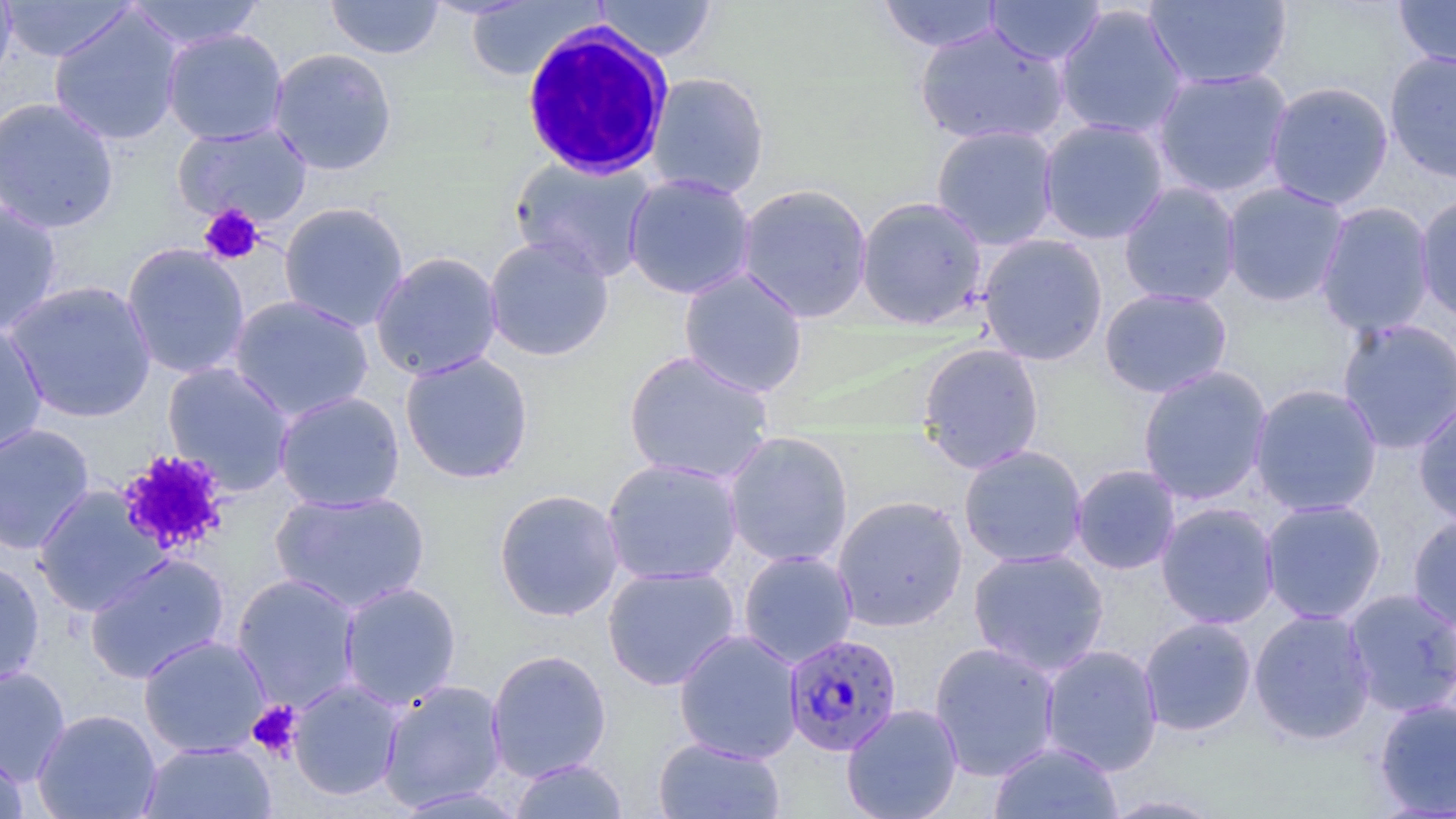 Approximate bounding boxes as (x1, y1, x2, y2) in pixels. Platelet locations: (198, 204, 265, 266), (115, 448, 232, 557), (245, 700, 303, 762). Uninfected red blood cell locations: (0, 0, 135, 63), (0, 0, 18, 91), (125, 0, 266, 51), (325, 0, 445, 60), (593, 0, 717, 62), (876, 0, 1004, 53), (1144, 0, 1293, 91), (1393, 0, 1456, 70), (463, 1, 602, 82), (986, 1, 1106, 65), (1054, 4, 1189, 140), (48, 7, 185, 147), (914, 23, 1070, 147), (161, 28, 289, 145), (267, 47, 398, 176), (1383, 50, 1456, 183), (1151, 67, 1294, 199), (645, 71, 771, 199), (1263, 80, 1395, 210), (0, 96, 120, 235), (1038, 118, 1170, 244), (172, 122, 313, 227), (931, 124, 1060, 250), (509, 155, 657, 282), (622, 172, 758, 300), (1221, 181, 1350, 308), (735, 182, 874, 323), (1118, 182, 1242, 308), (1415, 193, 1456, 324), (856, 196, 988, 329), (0, 198, 63, 337), (278, 201, 410, 332), (1315, 201, 1436, 337), (978, 233, 1108, 366), (483, 235, 614, 362), (120, 242, 251, 380), (369, 251, 504, 381), (678, 268, 809, 398), (3, 280, 158, 423), (1099, 287, 1233, 398), (228, 295, 375, 422), (1336, 317, 1456, 455), (0, 321, 48, 456), (917, 341, 1045, 474), (622, 349, 775, 485), (399, 351, 535, 484), (161, 361, 296, 495), (1137, 365, 1273, 505), (1249, 383, 1383, 517), (273, 390, 406, 512), (1413, 397, 1456, 526), (0, 422, 96, 554), (722, 430, 854, 569), (959, 445, 1088, 568), (601, 457, 744, 586), (1070, 464, 1181, 575), (32, 485, 170, 617), (493, 487, 626, 621), (270, 489, 431, 614), (831, 494, 969, 632), (1260, 499, 1387, 625), (1156, 502, 1280, 629), (1407, 513, 1456, 632), (967, 547, 1110, 676), (738, 550, 858, 668), (84, 552, 230, 684), (0, 559, 46, 689), (602, 565, 741, 690), (231, 573, 363, 711), (338, 580, 462, 710), (1342, 588, 1456, 718), (1248, 608, 1376, 745), (1138, 617, 1257, 736), (674, 628, 803, 764), (137, 633, 271, 757), (929, 641, 1062, 781), (1040, 645, 1163, 776), (485, 648, 612, 782), (0, 665, 71, 785), (288, 679, 407, 801), (377, 680, 507, 812), (1373, 698, 1456, 817), (841, 703, 963, 819), (31, 708, 162, 819), (652, 737, 787, 819), (138, 741, 277, 818), (988, 741, 1123, 819), (0, 746, 29, 819), (509, 758, 629, 818), (391, 786, 530, 817), (1097, 793, 1229, 818). White blood cell locations: (520, 22, 675, 180). Plasmodium falciparum-infected red blood cell locations: (782, 633, 902, 757). Slide-level diagnosis: Plasmodium falciparum. Single field of view. Thin blood smear. Captured at 1000x magnification. Image is 1456×819 pixels. Optical microscopy. May-Grünwald-Giemsa-stained preparation.